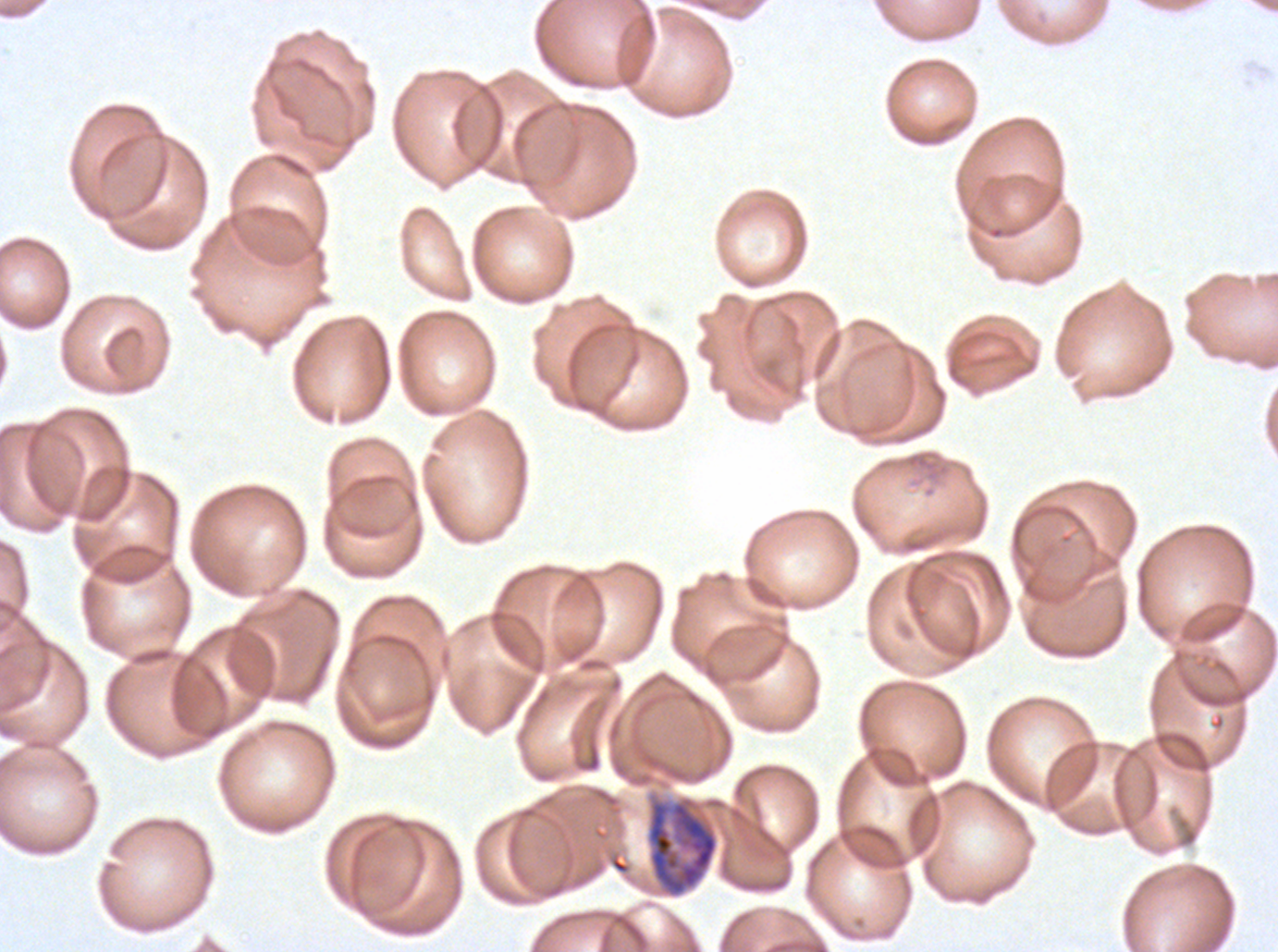
notation = approximate bounding boxes as [x1, y1, x2, y2] in pixels
late trophozoite locations = [646, 799, 719, 897]
preparation = thin blood smear
field of view = sub-image separated from a larger composite
stain = Giemsa
image size = 1278×952 pixels
specimen = ex-vivo P. falciparum culture from a patient in The Gambia, grown for 24 to 48 hours